Comment on the morphology of the red blood cells.
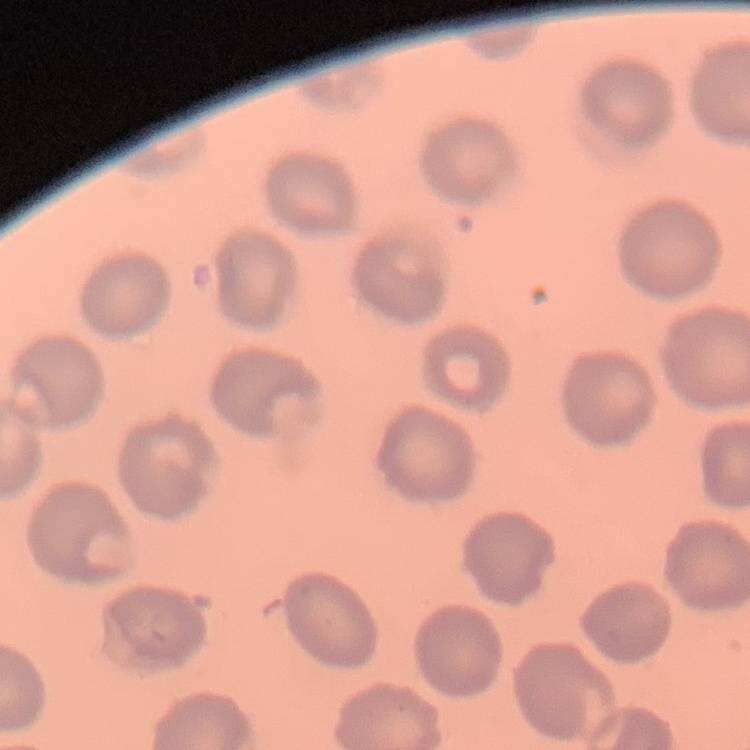
No rouleaux formation.

Field's or Giemsa stain. Square crop of a larger photomicrograph. Thin blood smear.